Assess the morphology of the erythrocytes.
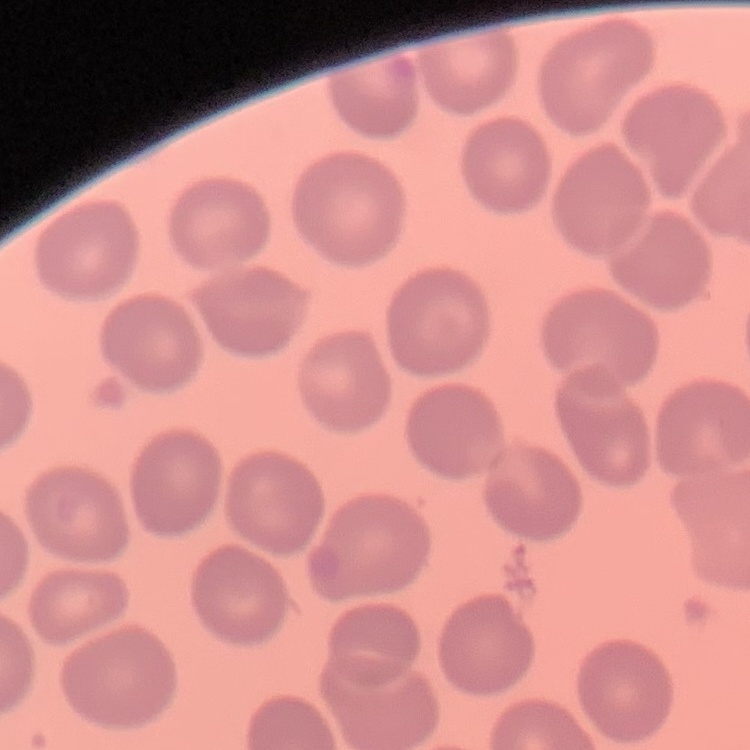

They show no rouleaux formation.

Square crop of a larger photomicrograph. Stained with either Field's or Giemsa. Thin blood film.